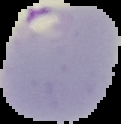

image size = 121×124 pixels
preparation = thin blood smear
result = Plasmodium parasites identified
image type = segmented cell region on a black background